Comment on the morphology of the red blood cells.
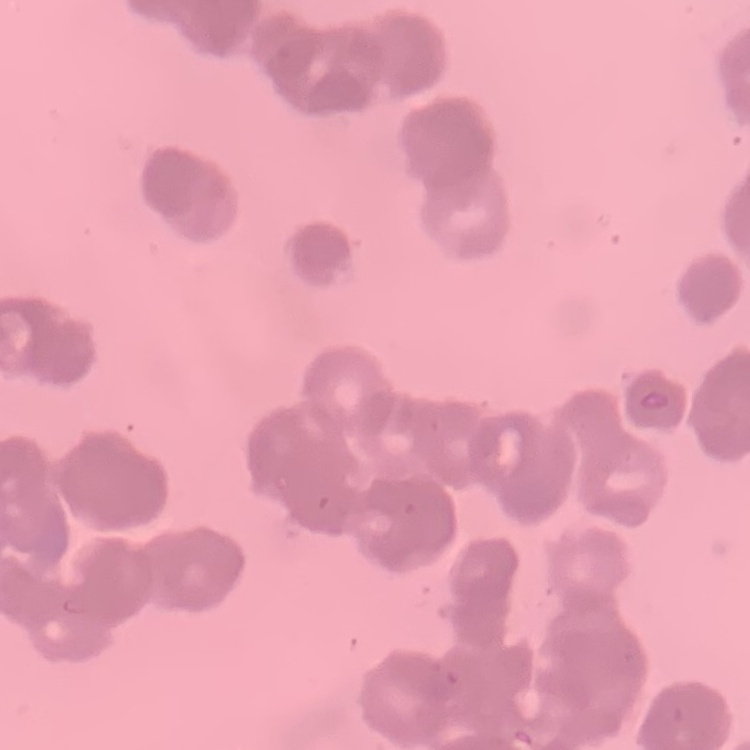

They show rouleaux formation.

{
  "preparation": "thin blood film",
  "stain": "Field's or Giemsa",
  "image_type": "one tile cut from a larger photomicrograph"
}